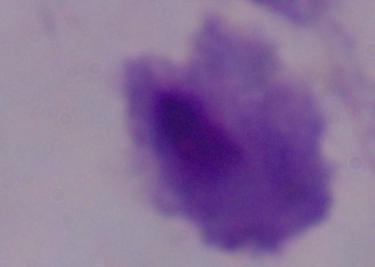
magnification: 1000x
identification: trichomonad
modality: photomicrograph